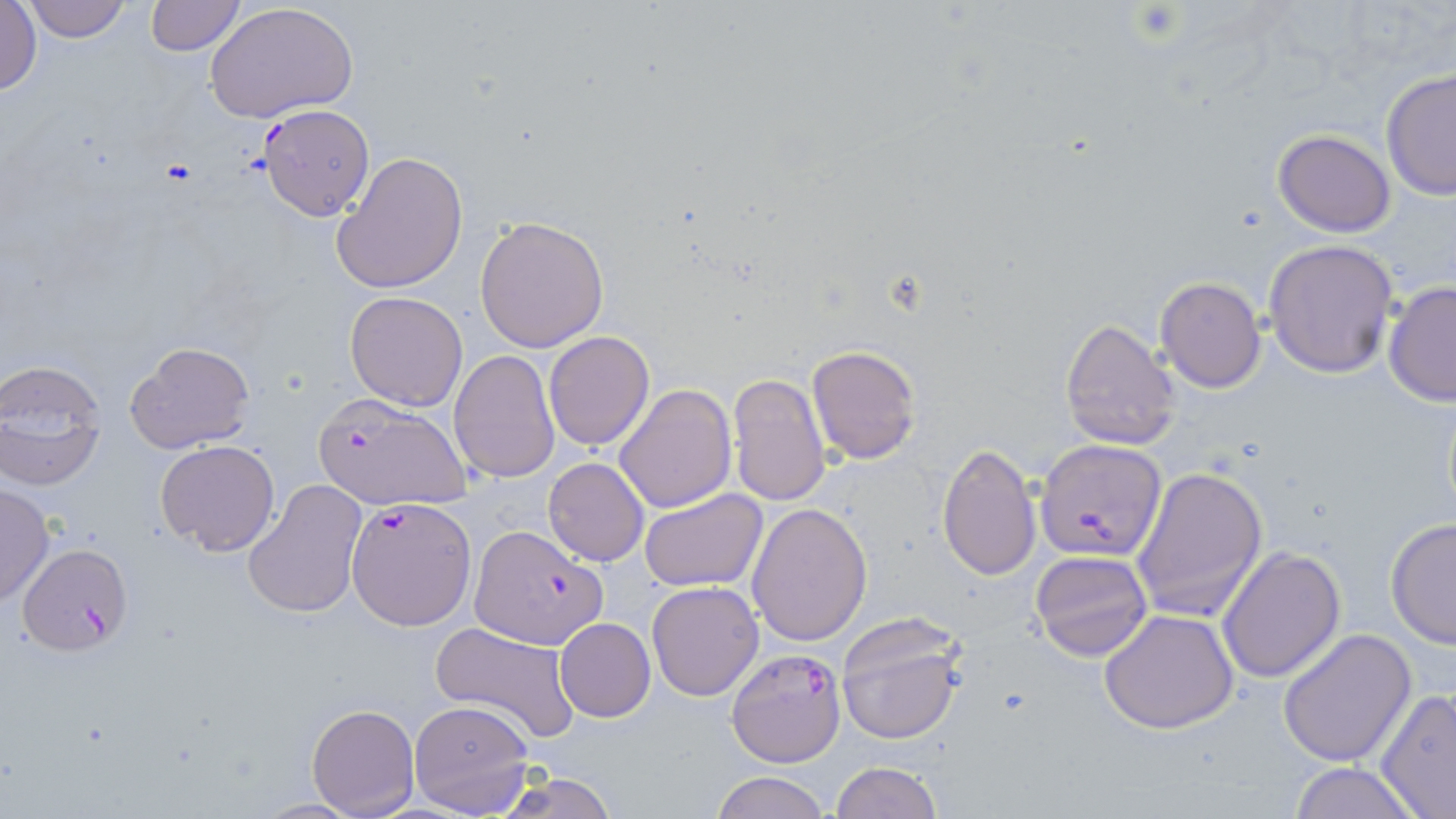
Summary:
  - Coordinate format: approximate bounding boxes as named x1/y1/x2/y2 corners in pixels
  - Uninfected red blood cell locations: (x1=24, y1=0, x2=133, y2=42), (x1=143, y1=0, x2=246, y2=55), (x1=203, y1=2, x2=357, y2=123), (x1=0, y1=3, x2=42, y2=98), (x1=1380, y1=67, x2=1456, y2=199), (x1=1272, y1=129, x2=1397, y2=238), (x1=333, y1=151, x2=468, y2=294), (x1=475, y1=216, x2=609, y2=353), (x1=1265, y1=239, x2=1399, y2=378), (x1=1155, y1=276, x2=1266, y2=393), (x1=1383, y1=281, x2=1456, y2=407), (x1=345, y1=290, x2=468, y2=410), (x1=1059, y1=319, x2=1181, y2=450), (x1=544, y1=331, x2=655, y2=452), (x1=125, y1=341, x2=256, y2=456), (x1=806, y1=344, x2=922, y2=465), (x1=448, y1=350, x2=559, y2=482), (x1=0, y1=357, x2=108, y2=490), (x1=728, y1=373, x2=832, y2=506), (x1=616, y1=384, x2=736, y2=512), (x1=155, y1=439, x2=280, y2=556), (x1=937, y1=441, x2=1041, y2=583), (x1=543, y1=457, x2=649, y2=566), (x1=1130, y1=465, x2=1269, y2=621), (x1=242, y1=478, x2=367, y2=619), (x1=0, y1=483, x2=54, y2=608), (x1=640, y1=490, x2=766, y2=593), (x1=746, y1=502, x2=873, y2=646), (x1=1384, y1=516, x2=1456, y2=650), (x1=1218, y1=546, x2=1347, y2=684), (x1=1030, y1=549, x2=1154, y2=661), (x1=645, y1=581, x2=764, y2=701), (x1=1099, y1=608, x2=1241, y2=733), (x1=834, y1=614, x2=965, y2=747), (x1=555, y1=618, x2=655, y2=721), (x1=429, y1=622, x2=581, y2=745), (x1=1276, y1=628, x2=1417, y2=767), (x1=1375, y1=688, x2=1456, y2=816), (x1=408, y1=699, x2=537, y2=817), (x1=307, y1=702, x2=419, y2=817), (x1=831, y1=761, x2=942, y2=819), (x1=1289, y1=761, x2=1421, y2=818), (x1=492, y1=771, x2=622, y2=819), (x1=712, y1=772, x2=832, y2=819)
  - Platelet locations: (x1=1128, y1=3, x2=1185, y2=42)
  - Plasmodium falciparum-infected red blood cell locations: (x1=258, y1=105, x2=374, y2=219), (x1=312, y1=392, x2=472, y2=509), (x1=1034, y1=437, x2=1168, y2=561), (x1=346, y1=497, x2=476, y2=630), (x1=470, y1=524, x2=607, y2=647), (x1=14, y1=542, x2=134, y2=654), (x1=727, y1=649, x2=848, y2=766)
  - Slide-level diagnosis: Plasmodium falciparum
  - Preparation: thin blood smear
  - Image size: 1456×819 pixels
  - Modality: optical microscopy
  - Field of view: single
  - Stain: May-Grünwald-Giemsa
  - Magnification: 1000x